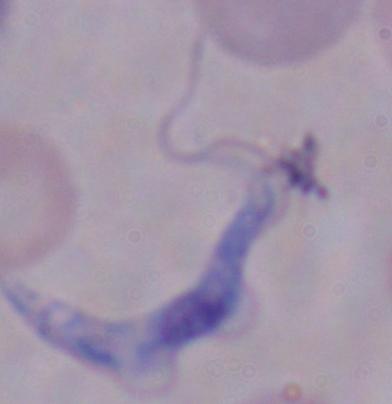
magnification = 1000x
modality = photomicrograph
identification = trypanosome